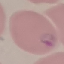
{
  "result": "malaria parasites detected",
  "image_type": "automatically extracted cell patch, resized to 64 × 64 pixels",
  "stain": "Giemsa",
  "capture": "smartphone camera at the microscope eyepiece",
  "preparation": "thin blood smear"
}